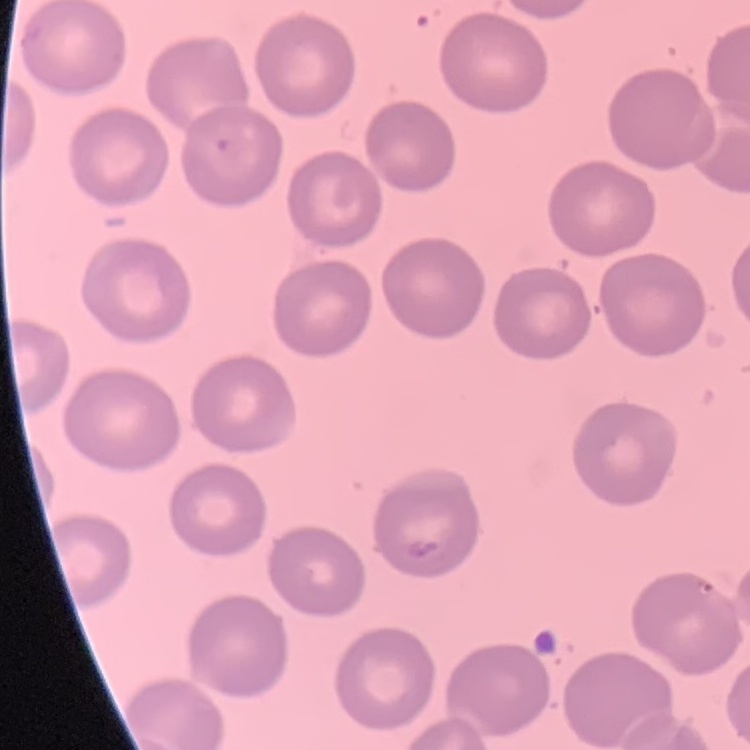
The red blood cells show no rouleaux formation. One tile cut from a larger photomicrograph. Stained with either Field's or Giemsa. Thin peripheral smear.